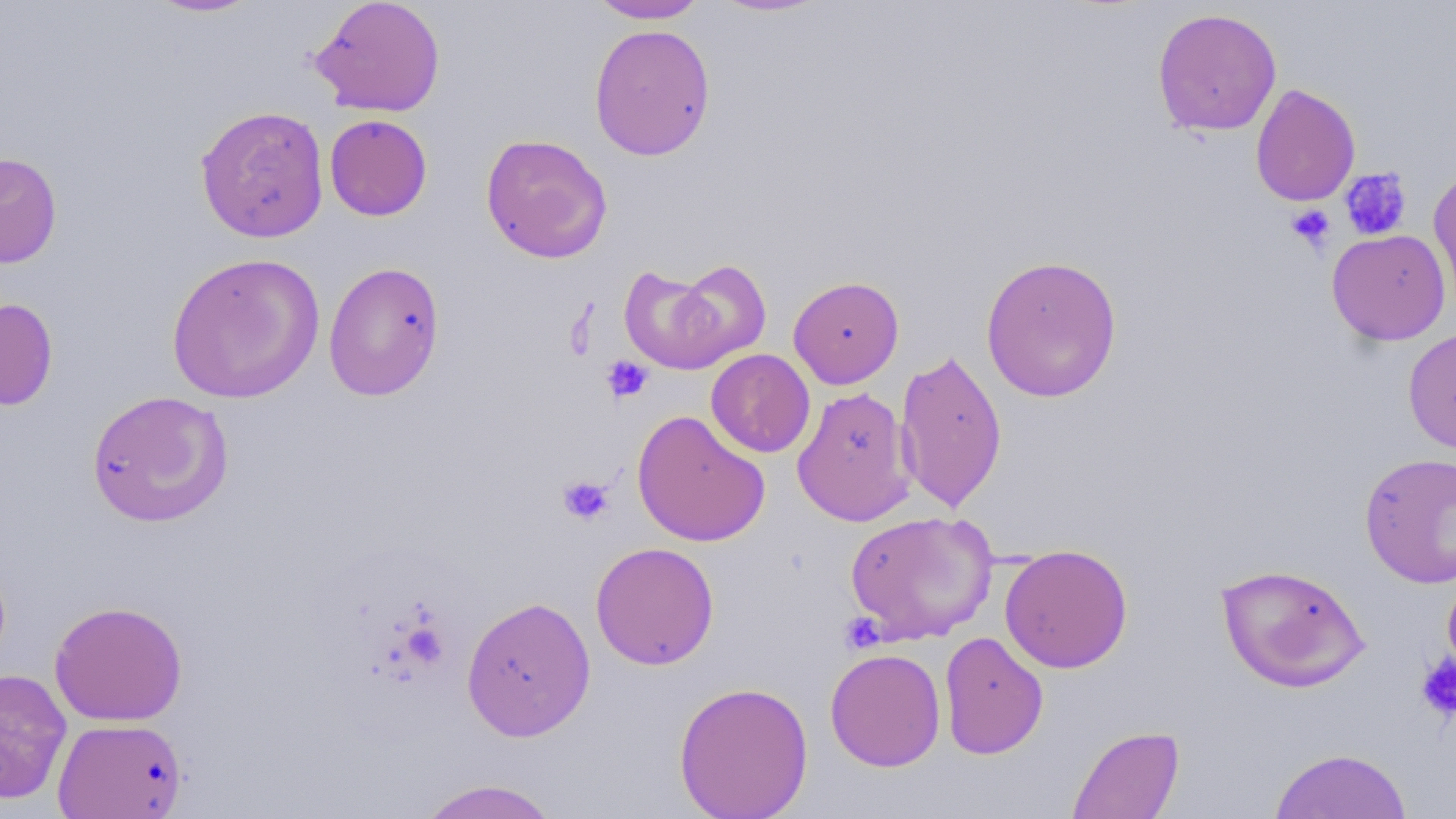
Summary:
  - Coordinate format: approximate bounding boxes as (x1, y1, x2, y2) in pixels
  - Platelet locations: (1339, 167, 1412, 240), (1286, 204, 1336, 254), (601, 356, 653, 403), (557, 475, 614, 526), (841, 613, 886, 653), (1416, 654, 1456, 721)
  - Uninfected red blood cell locations: (144, 0, 264, 18), (310, 0, 447, 117), (588, 0, 710, 24), (709, 0, 831, 18), (1151, 7, 1283, 136), (589, 23, 715, 161), (1250, 83, 1361, 207), (195, 105, 330, 243), (324, 114, 433, 221), (480, 133, 613, 263), (0, 151, 62, 269), (1429, 166, 1456, 306), (1327, 229, 1450, 345), (166, 251, 325, 404), (980, 254, 1122, 403), (669, 258, 771, 368), (323, 260, 445, 401), (619, 264, 734, 375), (788, 275, 904, 389), (0, 298, 58, 411), (1403, 327, 1456, 454), (895, 348, 1008, 513), (706, 349, 816, 458), (792, 386, 915, 527), (86, 390, 234, 528), (632, 410, 770, 547), (1359, 452, 1456, 589), (844, 510, 998, 644), (590, 541, 719, 670), (999, 543, 1133, 673), (1216, 562, 1370, 692), (1442, 568, 1456, 687), (460, 596, 596, 741), (49, 601, 188, 726), (938, 631, 1049, 760), (824, 648, 946, 771), (0, 668, 72, 805), (674, 679, 814, 819), (53, 717, 187, 819), (1068, 725, 1184, 818), (1269, 748, 1413, 819), (416, 778, 563, 819)
  - Slide-level diagnosis: no evidence of blood parasites
  - Modality: light microscopy
  - Image size: 1456×819 pixels
  - Stain: May-Grünwald-Giemsa
  - Magnification: 1000x
  - Preparation: thin blood film
  - Field of view: one of a larger specimen